Assess this cell for malaria.
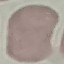

Uninfected.

Summary:
  - Capture: smartphone through the microscope eyepiece
  - Preparation: thin blood film
  - Stain: Giemsa
  - Image type: cell patch, automatically extracted from a larger field of view and resized to 64 × 64 pixels